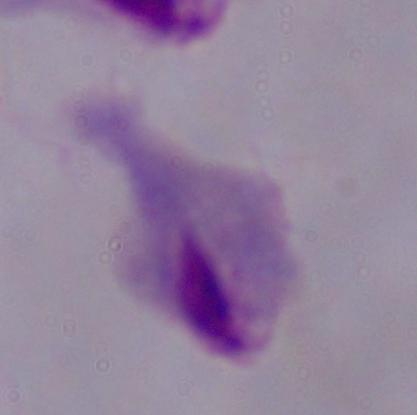
A trichomonad is shown. Captured at 1000x magnification. Micrograph.